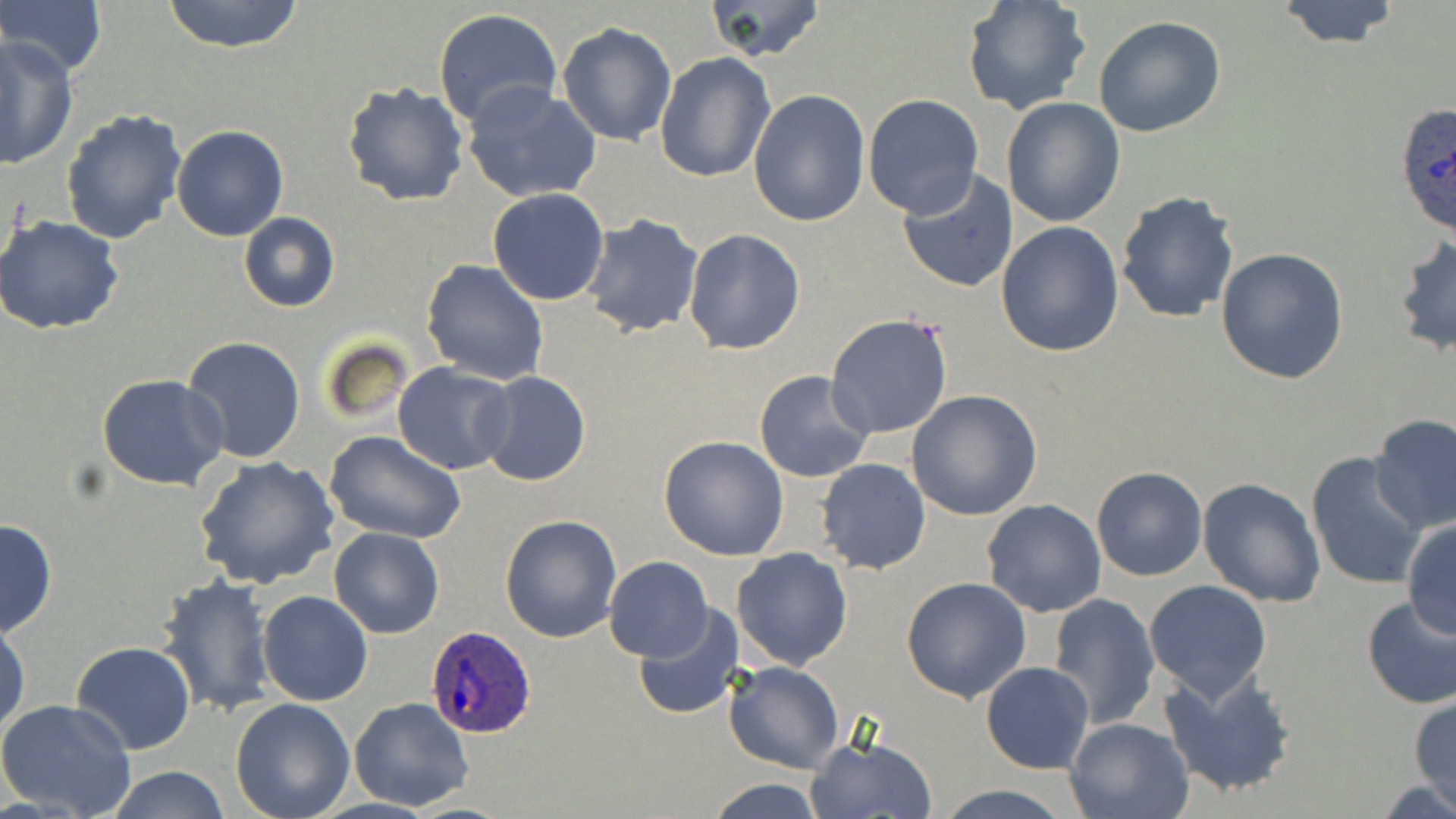
Approximate bounding boxes as [x1, y1, x2, y2] in pixels. Uninfected red blood cell locations: [0, 0, 107, 79], [161, 0, 307, 53], [703, 0, 827, 64], [962, 0, 1092, 116], [1274, 1, 1403, 50], [433, 8, 561, 130], [1092, 16, 1226, 138], [556, 21, 677, 147], [0, 37, 77, 169], [655, 51, 777, 184], [341, 81, 470, 208], [460, 82, 603, 205], [749, 91, 871, 228], [861, 93, 984, 219], [1002, 97, 1125, 227], [60, 108, 186, 247], [171, 125, 287, 241], [894, 168, 1020, 294], [487, 188, 610, 306], [1116, 190, 1239, 323], [238, 211, 340, 311], [1, 214, 124, 336], [581, 214, 703, 337], [997, 221, 1125, 358], [684, 228, 804, 354], [1393, 231, 1455, 358], [1216, 247, 1349, 383], [422, 260, 548, 386], [825, 314, 954, 440], [181, 335, 307, 464], [393, 363, 517, 475], [754, 370, 873, 483], [479, 371, 590, 488], [337, 374, 500, 530], [97, 375, 227, 491], [905, 390, 1042, 521], [1369, 413, 1456, 534], [323, 431, 466, 544], [659, 435, 789, 559], [1306, 453, 1427, 591], [194, 455, 340, 590], [816, 457, 930, 574], [1092, 467, 1207, 581], [1198, 478, 1327, 607], [982, 499, 1106, 619], [500, 515, 621, 644], [1402, 518, 1456, 641], [0, 519, 57, 638], [329, 527, 445, 639], [733, 547, 854, 668], [604, 556, 712, 660], [155, 573, 278, 718], [902, 576, 1032, 702], [1143, 580, 1273, 704], [258, 591, 373, 707], [1044, 593, 1161, 728], [1360, 594, 1456, 708], [632, 606, 742, 720], [0, 618, 29, 739], [70, 640, 195, 754], [724, 660, 844, 775], [981, 661, 1095, 775], [1158, 668, 1299, 796], [1408, 696, 1455, 808], [348, 697, 475, 810], [0, 698, 138, 819], [230, 698, 355, 819], [1065, 717, 1194, 819], [804, 734, 937, 819], [105, 765, 231, 819], [704, 777, 827, 819], [936, 784, 1073, 819]. Plasmodium ovale-infected red blood cell locations: [1396, 103, 1456, 237], [424, 625, 539, 739]. Slide-level diagnosis: Plasmodium ovale. Optical microscopy. Thin blood smear. Image is 1456×819 pixels. May-Grünwald-Giemsa-stained preparation. One field of a larger specimen. Captured at 1000x magnification.